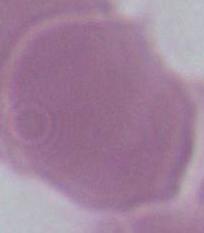

Summary:
  - Modality: micrograph
  - Magnification: 1000x
  - Identification: red blood cell